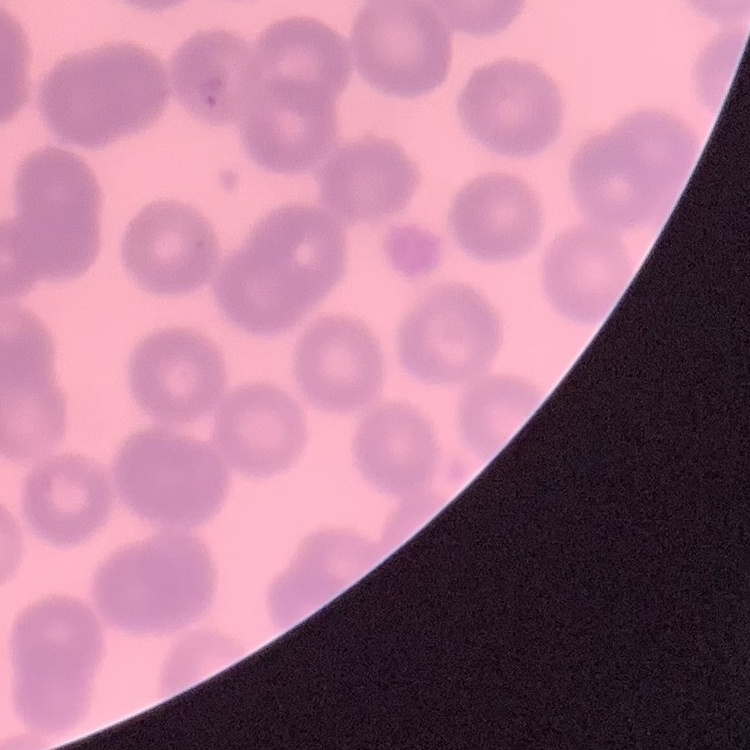
The red blood cells show no rouleaux formation. Square crop of a larger photomicrograph. Field's or Giemsa stain. Thin blood film.